Point out Plasmodium parasites and leukocytes.
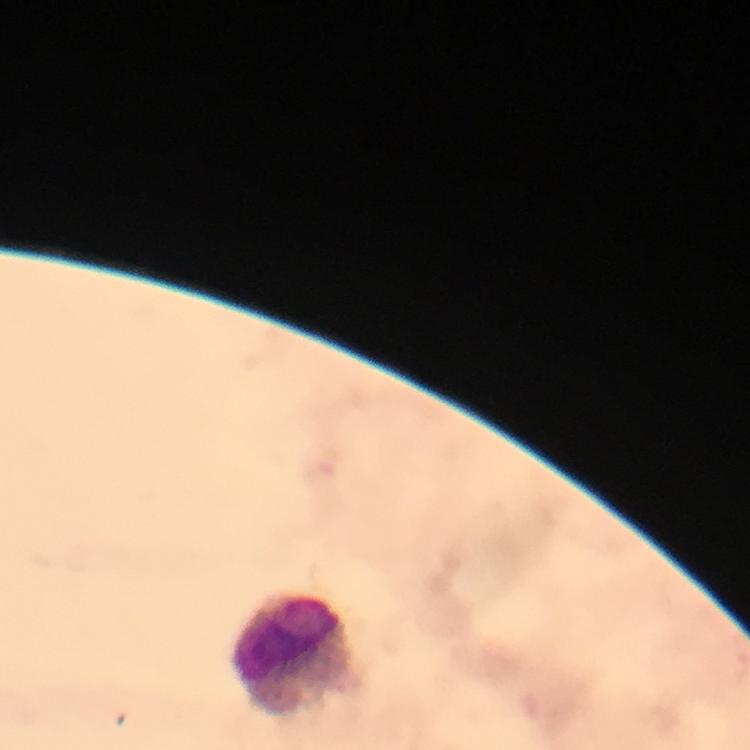
No Plasmodium parasites detected.
Approximate centers as (x, y) in pixels.
Leukocytes: (294, 652).

Summary:
  - Cropped from: one field of view
  - Context: from a diagnostic examination for malaria
  - Magnification: 100x
  - Preparation: thick smear
  - Capture: smartphone mounted on the microscope
  - Image size: 750×750 pixels
  - Immersion oil: used
  - Stain: Giemsa